Assess the morphology of the erythrocytes.
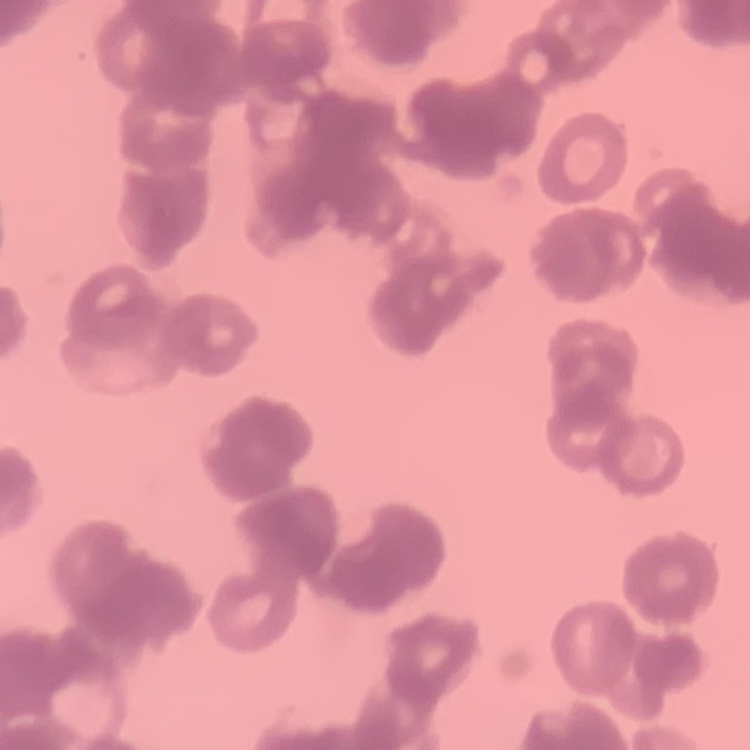
They show rouleaux formation.

Summary:
  - Stain: Field's or Giemsa
  - Preparation: thin blood smear
  - Image type: one tile cut from a larger photomicrograph